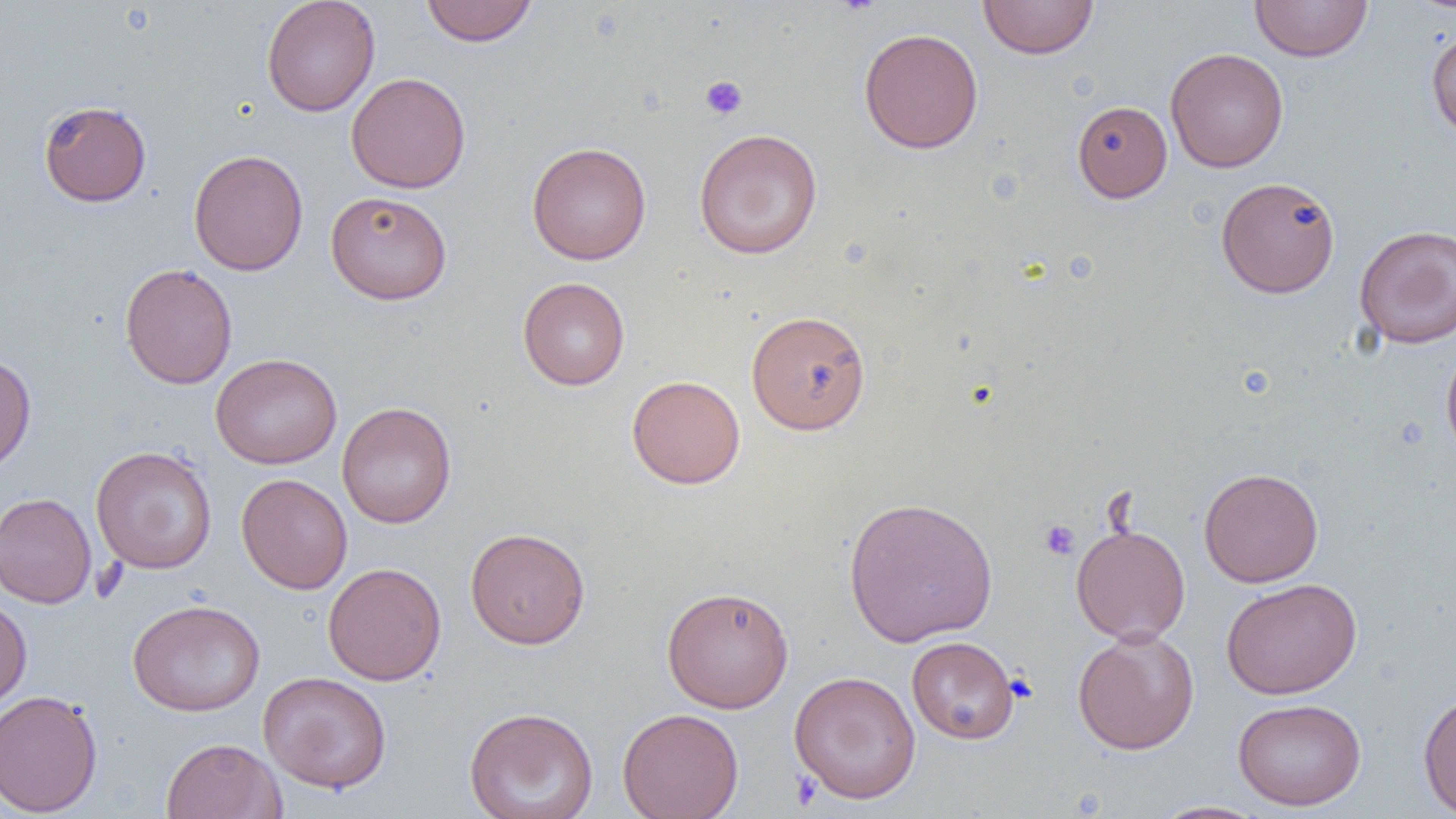

{
  "slide_level_diagnosis": "negative for blood parasites",
  "uninfected_red_blood_cell_locations": "approximate bounding boxes as (x1, y1, x2, y2) in pixels: (261, 0, 381, 116), (420, 0, 538, 46), (978, 0, 1099, 59), (1250, 1, 1372, 62), (858, 27, 984, 154), (1426, 27, 1456, 141), (1165, 47, 1289, 173), (345, 72, 471, 194), (38, 99, 152, 207), (1072, 100, 1172, 202), (694, 128, 823, 259), (527, 141, 652, 265), (188, 149, 308, 276), (1216, 176, 1340, 299), (325, 190, 453, 305), (1354, 223, 1456, 348), (120, 262, 237, 389), (517, 277, 630, 390), (746, 310, 871, 435), (1441, 342, 1456, 465), (0, 352, 37, 473), (210, 353, 342, 469), (626, 374, 746, 489), (337, 401, 457, 528), (90, 446, 217, 574), (1199, 467, 1323, 587), (236, 473, 353, 594), (0, 492, 97, 609), (843, 496, 998, 647), (1071, 523, 1191, 644), (465, 527, 591, 650), (322, 562, 447, 686), (1220, 578, 1361, 699), (661, 586, 794, 712), (0, 595, 32, 712), (127, 598, 265, 716), (1072, 628, 1200, 754), (906, 636, 1019, 744), (788, 670, 922, 804), (258, 671, 392, 794), (0, 689, 104, 817), (1418, 690, 1456, 817), (1232, 697, 1366, 811), (464, 707, 599, 818), (617, 707, 745, 819), (160, 737, 286, 819), (1149, 800, 1272, 819)",
  "magnification": "1000x",
  "field_of_view": "single",
  "platelet_locations": "approximate bounding boxes as (x1, y1, x2, y2) in pixels: (833, 0, 881, 16), (699, 75, 748, 120), (1039, 519, 1080, 560), (789, 770, 822, 810)",
  "modality": "optical microscopy",
  "preparation": "thin blood film",
  "image_size": "1456×819 pixels"
}